Assess this cell for malaria.
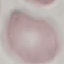
Uninfected.

Thin blood film. Giemsa-stained preparation. Acquired by smartphone through the microscope eyepiece. Cell patch, automatically extracted from a larger field of view and resized to 64 × 64 pixels.